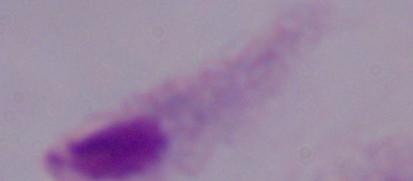
Captured at 1000x magnification. A trichomonad is shown. Micrograph.